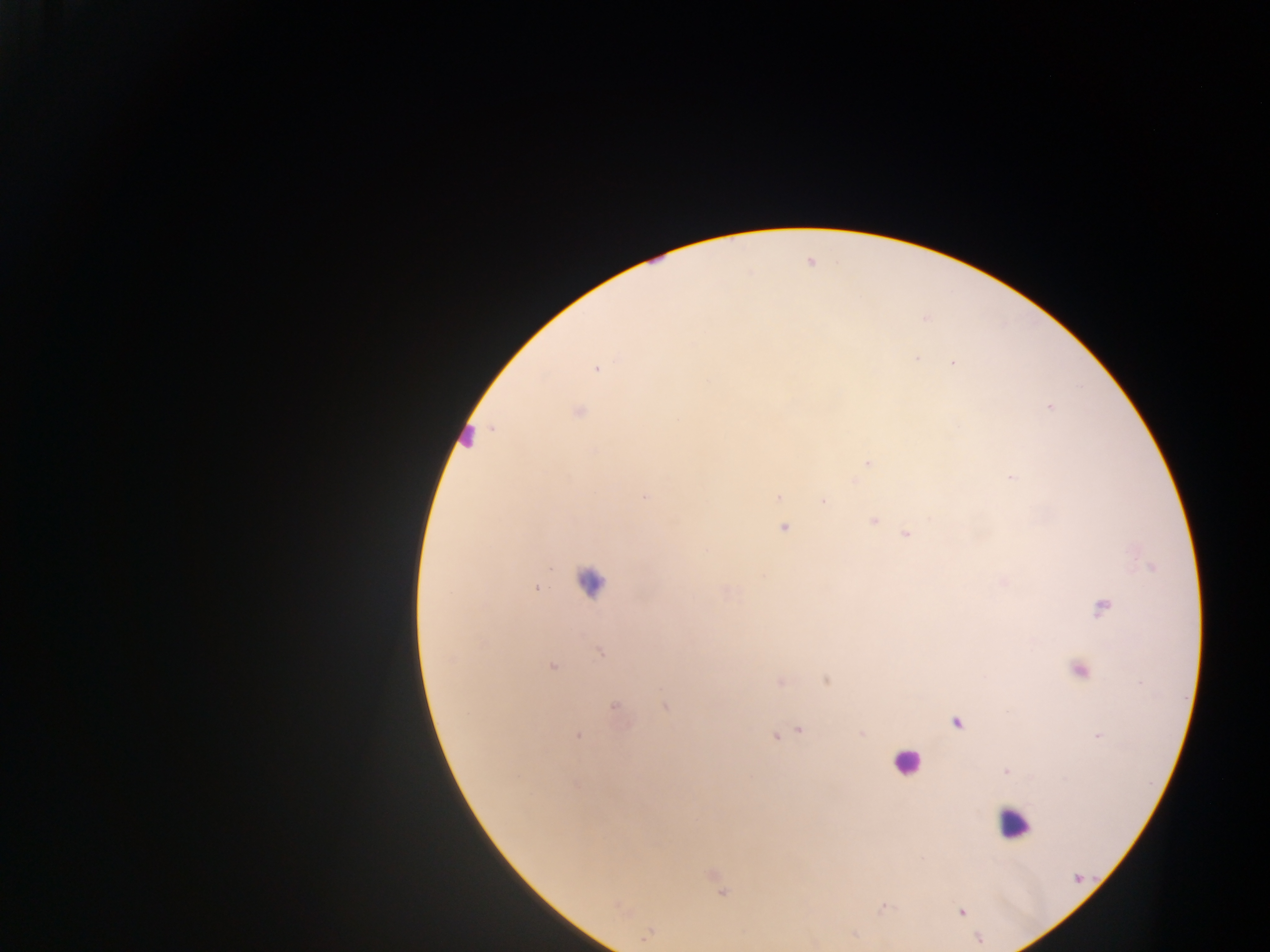

Approximate centers as x y in pixels.
Summary:
  - Leukocyte locations: 467 435; 590 582; 907 763; 1013 823
  - Malaria parasite locations: 952 362; 598 368; 1049 407; 577 411; 868 462; 1011 477; 645 496; 778 496; 823 501; 873 519; 784 527; 907 534; 536 588; 1102 606; 600 651; 552 666; 1078 670; 827 679; 781 682; 666 705; 615 708; 956 722; 799 730; 861 733; 578 735; 774 736; 1097 736; 1006 771; 713 877; 722 891; 884 907; 962 912; 647 935; 813 942
  - Preparation: thick blood smear
  - Image size: 1270×952 pixels
  - Field of view: single
  - Capture: mobile-phone photograph through a microscope
  - Country: Ghana